State which cell type is depicted.
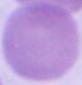
An erythrocyte.

Micrograph. Captured at 1000x magnification.